State which parasite is depicted.
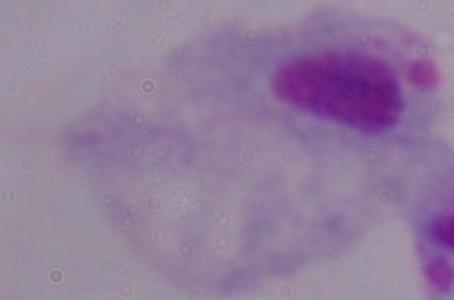
This is a trichomonad.

Summary:
  - Modality: photomicrograph
  - Magnification: 1000x